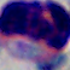
identification: white blood cell
magnification: 1000x
modality: photomicrograph